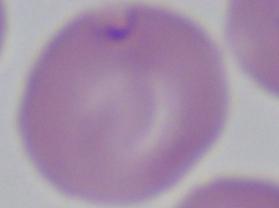

identification: Babesia
modality: photomicrograph
magnification: 1000x